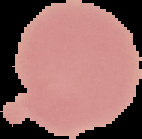
{
  "image_size": "142×139 pixels",
  "image_type": "segmented cell region with the area outside set to black",
  "result": "no Plasmodium parasites detected",
  "preparation": "thin blood smear"
}